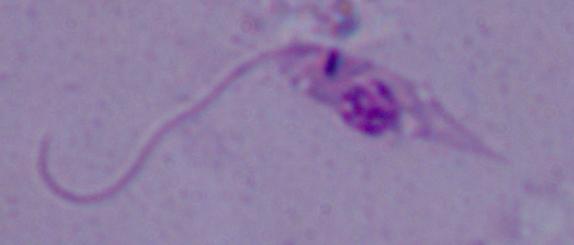
A Leishmania parasite is seen. 1000x magnification. Photomicrograph.